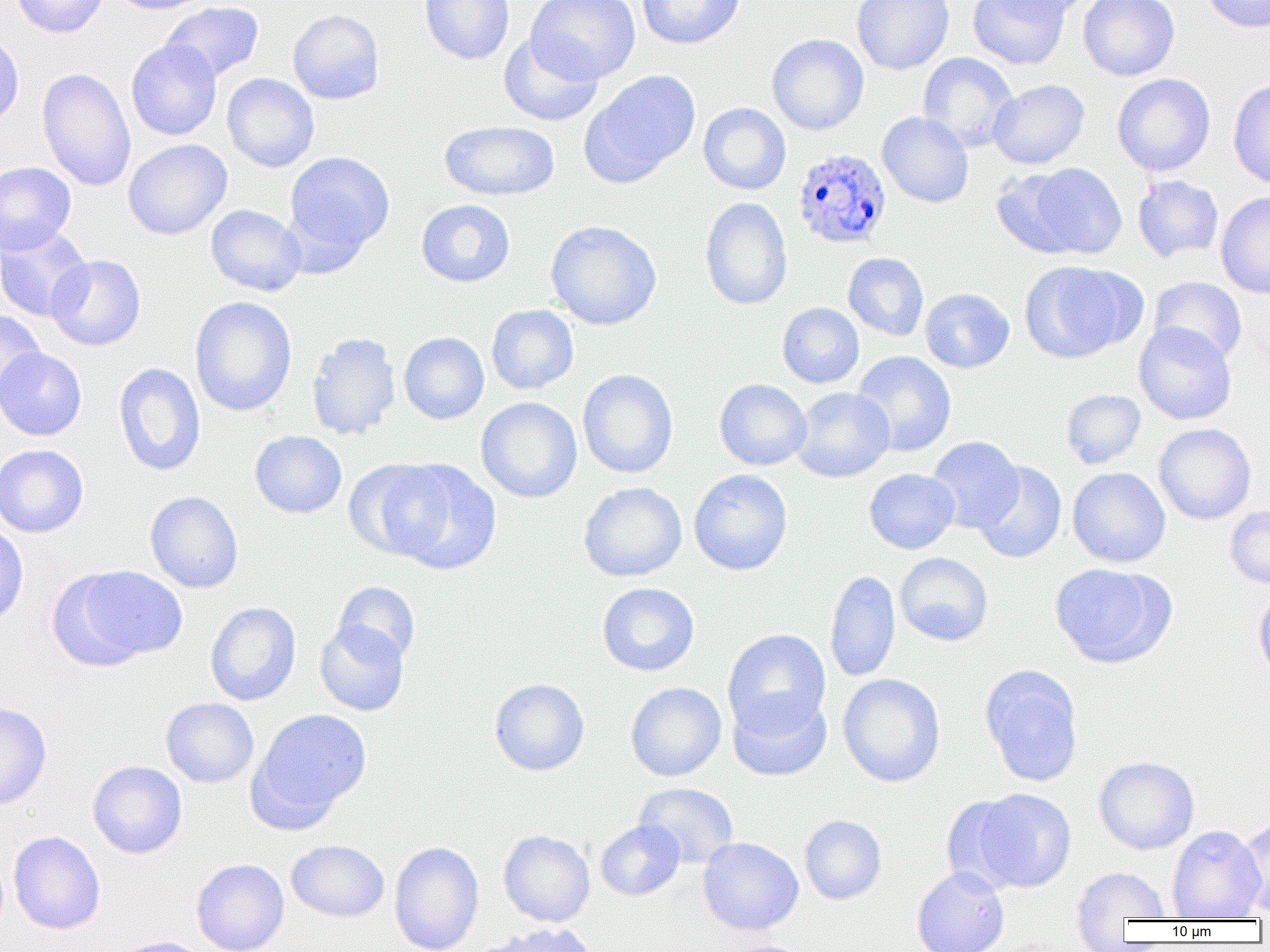

Approximate bounding boxes as (x1, y1, x2, y2) in pixels. Plasmodium ovale-infected red blood cell locations: (792, 147, 891, 249). Uninfected red blood cell locations: (11, 0, 109, 38), (107, 0, 214, 15), (420, 0, 514, 64), (527, 0, 641, 83), (637, 0, 745, 50), (852, 0, 954, 75), (968, 0, 1071, 69), (988, 0, 1096, 20), (1078, 0, 1180, 80), (1200, 0, 1270, 33), (161, 1, 264, 83), (288, 9, 385, 104), (498, 32, 604, 126), (0, 33, 24, 133), (767, 34, 869, 135), (126, 39, 222, 140), (917, 52, 1018, 151), (37, 67, 136, 192), (580, 70, 701, 187), (222, 73, 319, 172), (1112, 74, 1215, 176), (1228, 77, 1270, 189), (988, 78, 1089, 168), (698, 102, 791, 195), (877, 112, 974, 208), (440, 120, 559, 201), (123, 139, 232, 240), (284, 151, 395, 255), (0, 162, 76, 254), (1022, 162, 1127, 260), (991, 168, 1088, 258), (1132, 175, 1224, 262), (1216, 191, 1270, 298), (700, 196, 793, 311), (416, 199, 515, 287), (206, 204, 306, 296), (545, 220, 662, 330), (0, 225, 92, 323), (843, 252, 929, 341), (46, 254, 146, 350), (1020, 261, 1138, 363), (1148, 276, 1247, 364), (919, 288, 1014, 373), (189, 296, 297, 417), (778, 302, 864, 388), (486, 304, 579, 394), (0, 309, 46, 406), (1134, 322, 1237, 424), (306, 332, 401, 440), (399, 332, 489, 424), (0, 347, 87, 441), (851, 351, 956, 457), (114, 362, 206, 476), (577, 368, 678, 478), (714, 378, 812, 470), (791, 387, 894, 482), (1061, 389, 1146, 469), (1063, 389, 1153, 558), (476, 397, 582, 503), (1154, 423, 1256, 524), (249, 431, 347, 518), (927, 436, 1024, 532), (0, 444, 89, 537), (346, 459, 456, 562), (389, 460, 501, 574), (973, 461, 1067, 564), (1068, 467, 1170, 567), (864, 468, 960, 554), (689, 469, 792, 575), (578, 481, 687, 582), (145, 491, 243, 592), (1225, 505, 1270, 589), (0, 521, 28, 626), (895, 552, 993, 646), (1050, 563, 1169, 667), (71, 564, 188, 663), (824, 570, 900, 682), (333, 581, 421, 665), (597, 582, 699, 676), (1252, 588, 1270, 682), (205, 601, 301, 706), (315, 620, 410, 717), (723, 628, 830, 735), (980, 666, 1084, 787), (837, 673, 945, 787), (489, 678, 589, 776), (625, 682, 726, 781), (728, 689, 831, 781), (161, 698, 259, 787), (0, 702, 52, 810), (252, 708, 371, 821), (1094, 756, 1199, 855), (88, 761, 187, 858), (634, 782, 738, 868), (971, 788, 1077, 892), (941, 796, 1027, 894), (799, 815, 886, 904), (1233, 816, 1270, 918), (595, 820, 685, 900), (1167, 824, 1266, 919), (498, 830, 595, 927), (8, 831, 105, 935), (698, 837, 804, 936), (286, 840, 389, 922), (389, 841, 484, 952), (191, 859, 289, 952), (911, 866, 1009, 952), (1072, 867, 1170, 926), (479, 922, 598, 952), (108, 936, 212, 952), (716, 939, 818, 952). Slide-level diagnosis: Plasmodium ovale. Thin blood smear. Single field of view. Captured at 1000x magnification. Image is 1270×952 pixels. Light microscopy.